Identify the cell.
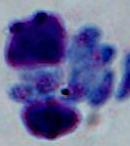

This is a leukocyte.

Summary:
  - Magnification: 1000x
  - Modality: photomicrograph